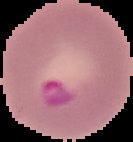

Summary:
  - Result: Plasmodium parasites detected
  - Image size: 133×142 pixels
  - Image type: segmented cell region with the area outside set to black
  - Preparation: thin blood smear